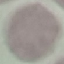

malaria_status: uninfected
capture: smartphone through the microscope eyepiece
image_type: automatically extracted cell patch, resized to 64 × 64 pixels
preparation: thin blood film
stain: Giemsa